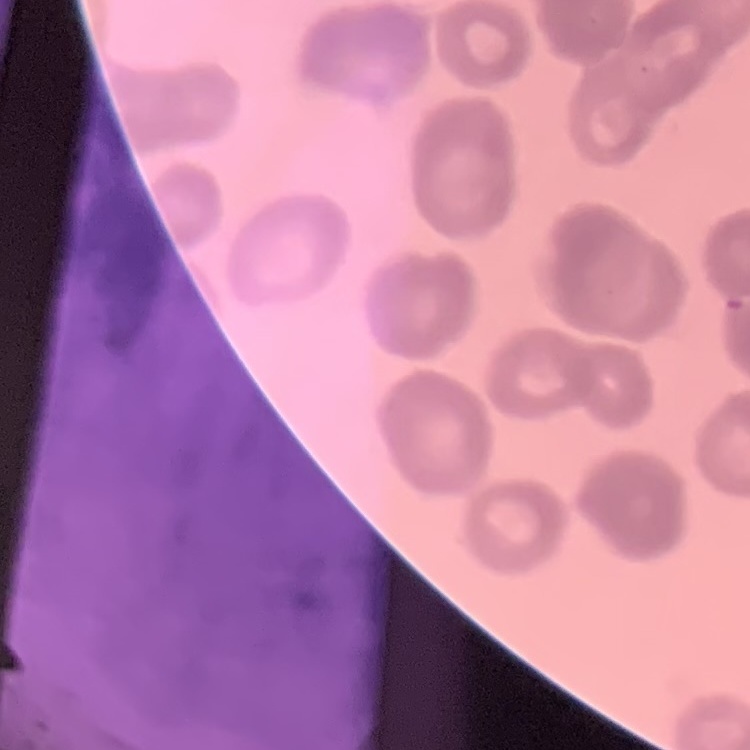

{
  "erythrocyte_morphology": "rouleaux formation",
  "image_type": "one tile cut from a larger photomicrograph",
  "stain": "Field's or Giemsa",
  "preparation": "thin peripheral smear"
}